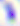
Summary:
  - Magnification: 400x
  - Modality: micrograph
  - Identification: Toxoplasma gondii